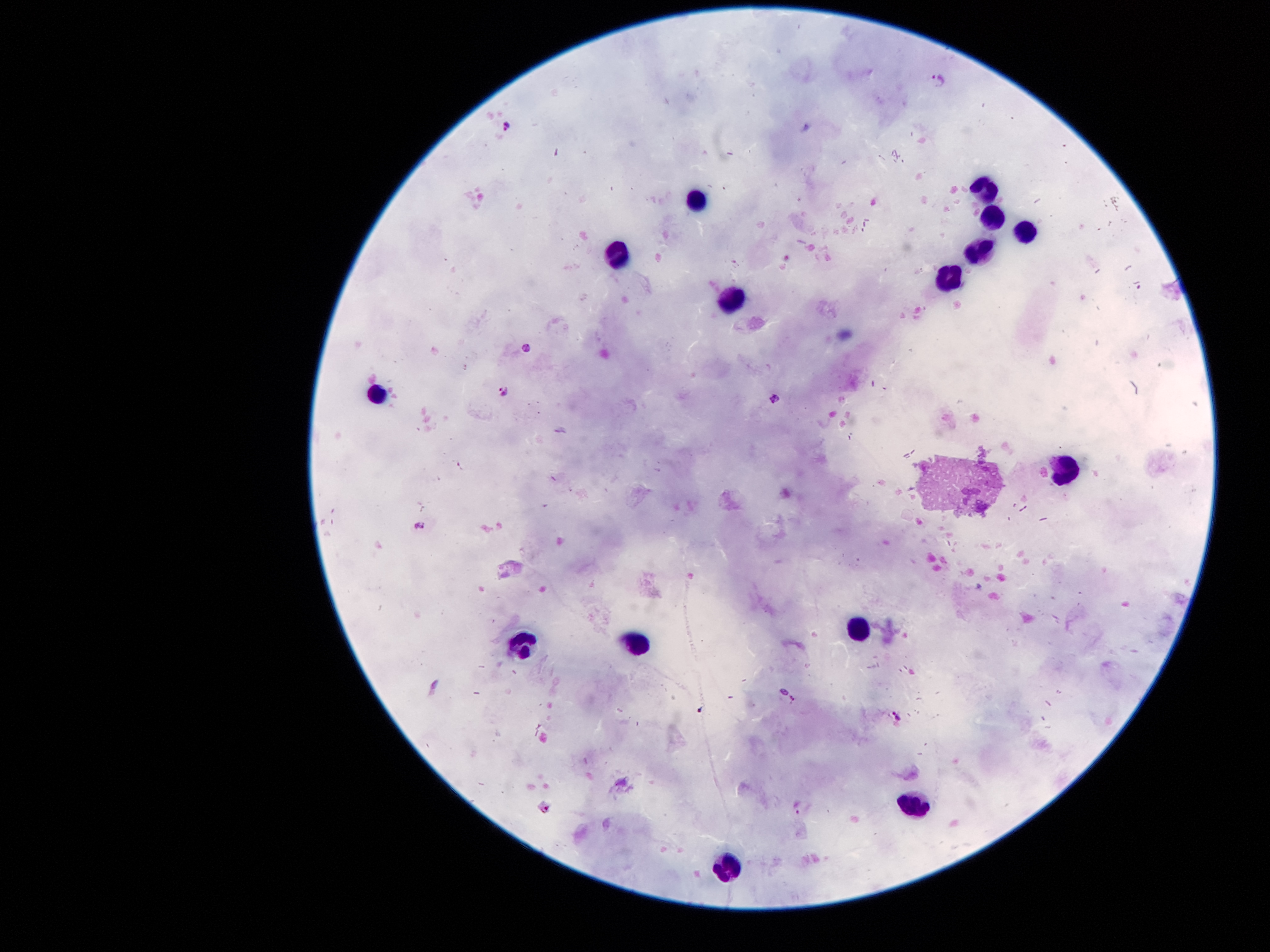

Approximate centers as (x, y) in pixels. Plasmodium parasite locations: (938, 79), (508, 127), (525, 348), (501, 391), (772, 399), (421, 523), (701, 710), (896, 717), (798, 806), (545, 808). Leukocyte locations: (982, 189), (696, 200), (987, 212), (1026, 230), (980, 249), (616, 256), (953, 273), (730, 301), (377, 394), (1068, 461), (856, 627), (525, 644), (637, 644), (916, 803), (726, 868). Patient malaria status: infected with Plasmodium falciparum. 100x magnification. Giemsa-stained preparation. Thick peripheral-blood smear. Image is 1270×952 pixels. One field from this slide. Smartphone photograph taken through the microscope eyepiece.